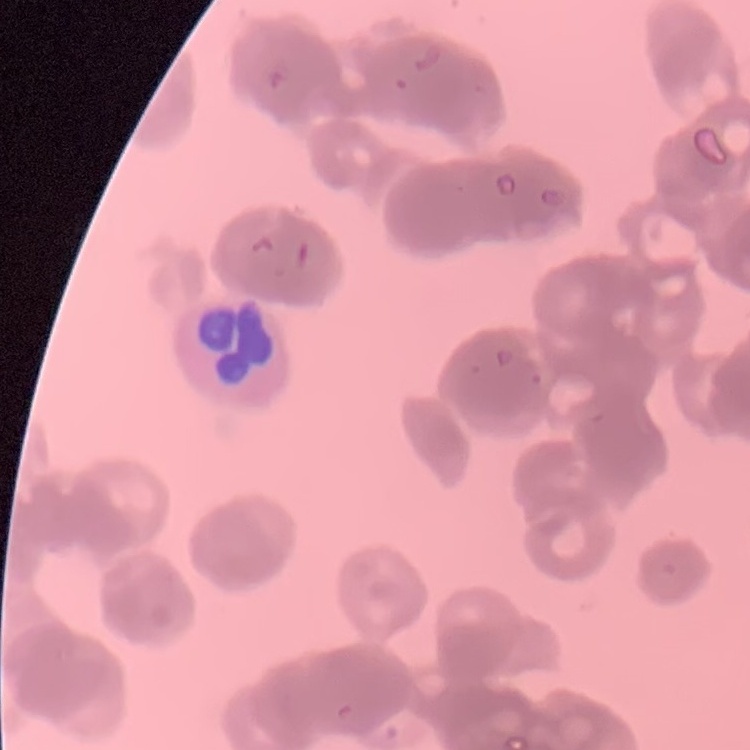
The erythrocytes show rouleaux formation. Thin blood film. Field's or Giemsa stain. One tile cut from a larger photomicrograph.